Identify the parasite.
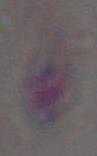

This is Toxoplasma gondii.

1000x magnification. Photomicrograph.